Outline each blood parasite and name the species.
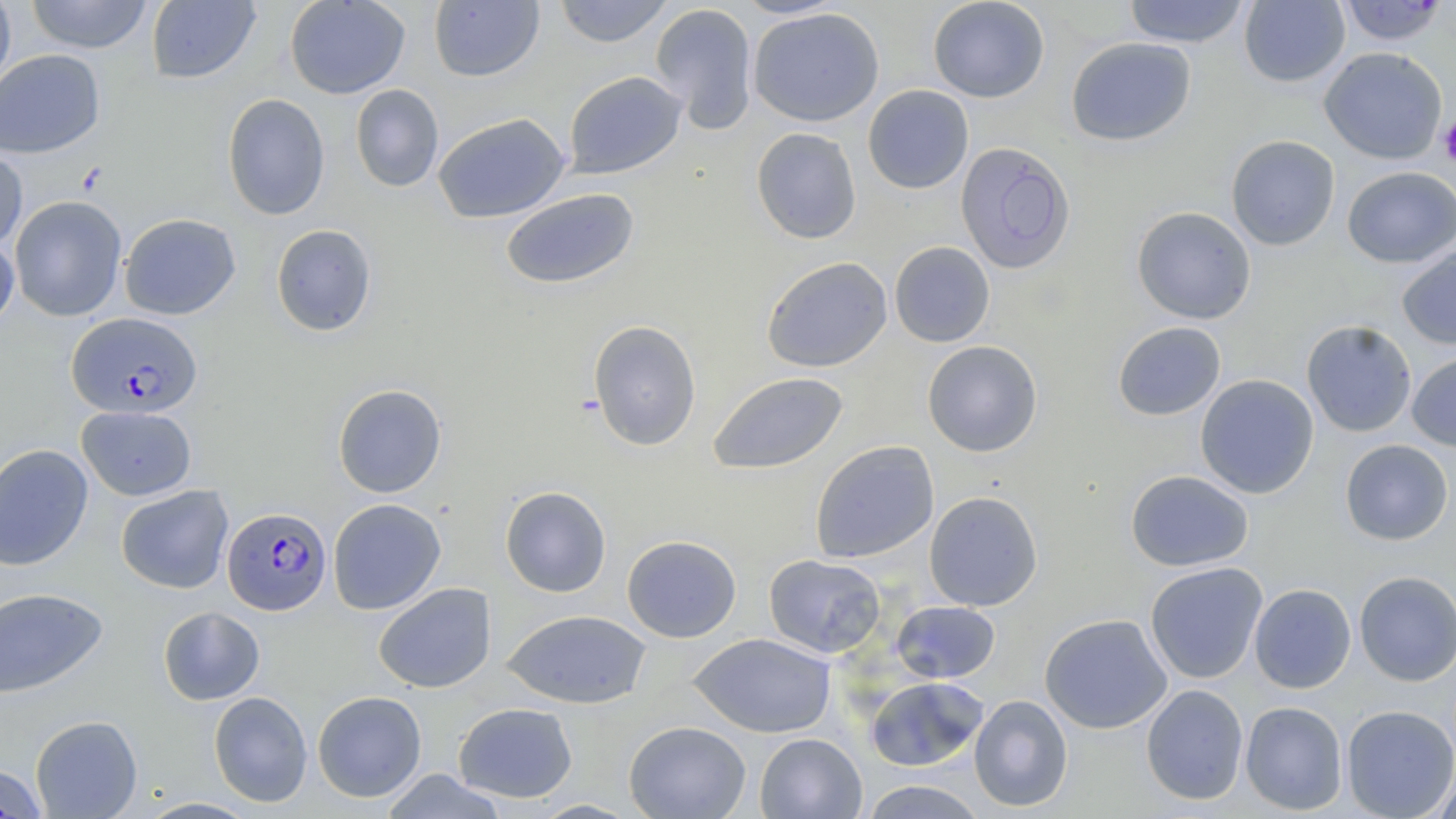
Approximate bounding boxes as named x1/y1/x2/y2 corners in pixels.
Plasmodium falciparum-infected red blood cells: (x1=66, y1=312, x2=202, y2=418), (x1=222, y1=506, x2=332, y2=615).
No Plasmodium ovale, Plasmodium malariae, Plasmodium vivax, Babesia divergens, or Trypanosoma brucei observed.

Uninfected red blood cell locations: (x1=0, y1=0, x2=16, y2=98), (x1=25, y1=0, x2=154, y2=53), (x1=145, y1=0, x2=261, y2=84), (x1=284, y1=0, x2=410, y2=99), (x1=553, y1=0, x2=674, y2=47), (x1=734, y1=0, x2=847, y2=19), (x1=927, y1=0, x2=1050, y2=103), (x1=1122, y1=0, x2=1251, y2=48), (x1=1239, y1=0, x2=1350, y2=88), (x1=1337, y1=0, x2=1450, y2=46), (x1=429, y1=1, x2=544, y2=83), (x1=649, y1=2, x2=758, y2=134), (x1=748, y1=7, x2=885, y2=127), (x1=1066, y1=37, x2=1196, y2=146), (x1=1319, y1=47, x2=1448, y2=164), (x1=0, y1=49, x2=105, y2=158), (x1=563, y1=71, x2=687, y2=179), (x1=349, y1=84, x2=444, y2=192), (x1=862, y1=85, x2=974, y2=194), (x1=222, y1=93, x2=330, y2=220), (x1=433, y1=112, x2=570, y2=224), (x1=751, y1=127, x2=861, y2=245), (x1=1226, y1=135, x2=1340, y2=251), (x1=955, y1=142, x2=1075, y2=275), (x1=0, y1=147, x2=28, y2=251), (x1=1342, y1=166, x2=1456, y2=268), (x1=500, y1=188, x2=639, y2=289), (x1=10, y1=195, x2=127, y2=321), (x1=1131, y1=206, x2=1256, y2=324), (x1=119, y1=213, x2=241, y2=320), (x1=271, y1=223, x2=377, y2=337), (x1=0, y1=232, x2=19, y2=332), (x1=889, y1=241, x2=995, y2=347), (x1=1397, y1=245, x2=1456, y2=350), (x1=761, y1=256, x2=892, y2=372), (x1=588, y1=320, x2=702, y2=451), (x1=1301, y1=320, x2=1417, y2=437), (x1=1112, y1=321, x2=1226, y2=421), (x1=922, y1=340, x2=1043, y2=457), (x1=1407, y1=350, x2=1456, y2=452), (x1=707, y1=371, x2=848, y2=475), (x1=1195, y1=374, x2=1319, y2=498), (x1=332, y1=383, x2=447, y2=498), (x1=76, y1=405, x2=196, y2=500), (x1=1340, y1=439, x2=1453, y2=545), (x1=810, y1=440, x2=939, y2=563), (x1=0, y1=443, x2=93, y2=571), (x1=1125, y1=470, x2=1254, y2=572), (x1=115, y1=485, x2=234, y2=594), (x1=500, y1=485, x2=612, y2=597), (x1=924, y1=490, x2=1043, y2=611), (x1=327, y1=498, x2=446, y2=615), (x1=621, y1=534, x2=741, y2=643), (x1=763, y1=554, x2=885, y2=658), (x1=1145, y1=562, x2=1268, y2=683), (x1=1353, y1=570, x2=1456, y2=685), (x1=374, y1=582, x2=496, y2=693), (x1=1249, y1=584, x2=1356, y2=693), (x1=0, y1=588, x2=109, y2=698), (x1=891, y1=601, x2=1000, y2=683), (x1=158, y1=606, x2=265, y2=705), (x1=501, y1=609, x2=652, y2=709), (x1=1039, y1=614, x2=1172, y2=733), (x1=688, y1=632, x2=835, y2=738), (x1=865, y1=676, x2=988, y2=771), (x1=1141, y1=684, x2=1248, y2=805), (x1=312, y1=690, x2=427, y2=802), (x1=208, y1=691, x2=313, y2=807), (x1=969, y1=695, x2=1073, y2=812), (x1=1240, y1=701, x2=1348, y2=815), (x1=453, y1=702, x2=578, y2=802), (x1=1341, y1=705, x2=1456, y2=819), (x1=30, y1=714, x2=143, y2=818), (x1=624, y1=720, x2=751, y2=819), (x1=754, y1=733, x2=867, y2=818), (x1=0, y1=763, x2=48, y2=818), (x1=1432, y1=764, x2=1456, y2=819), (x1=380, y1=769, x2=508, y2=818), (x1=858, y1=780, x2=988, y2=818), (x1=136, y1=797, x2=262, y2=818), (x1=532, y1=799, x2=640, y2=818). Platelet locations: (x1=1438, y1=115, x2=1456, y2=168). Slide-level diagnosis: Plasmodium falciparum. Optical microscopy. Captured at 1000x magnification. One field of a larger specimen. May-Grünwald-Giemsa-stained preparation. Thin blood film. Image is 1456×819 pixels.